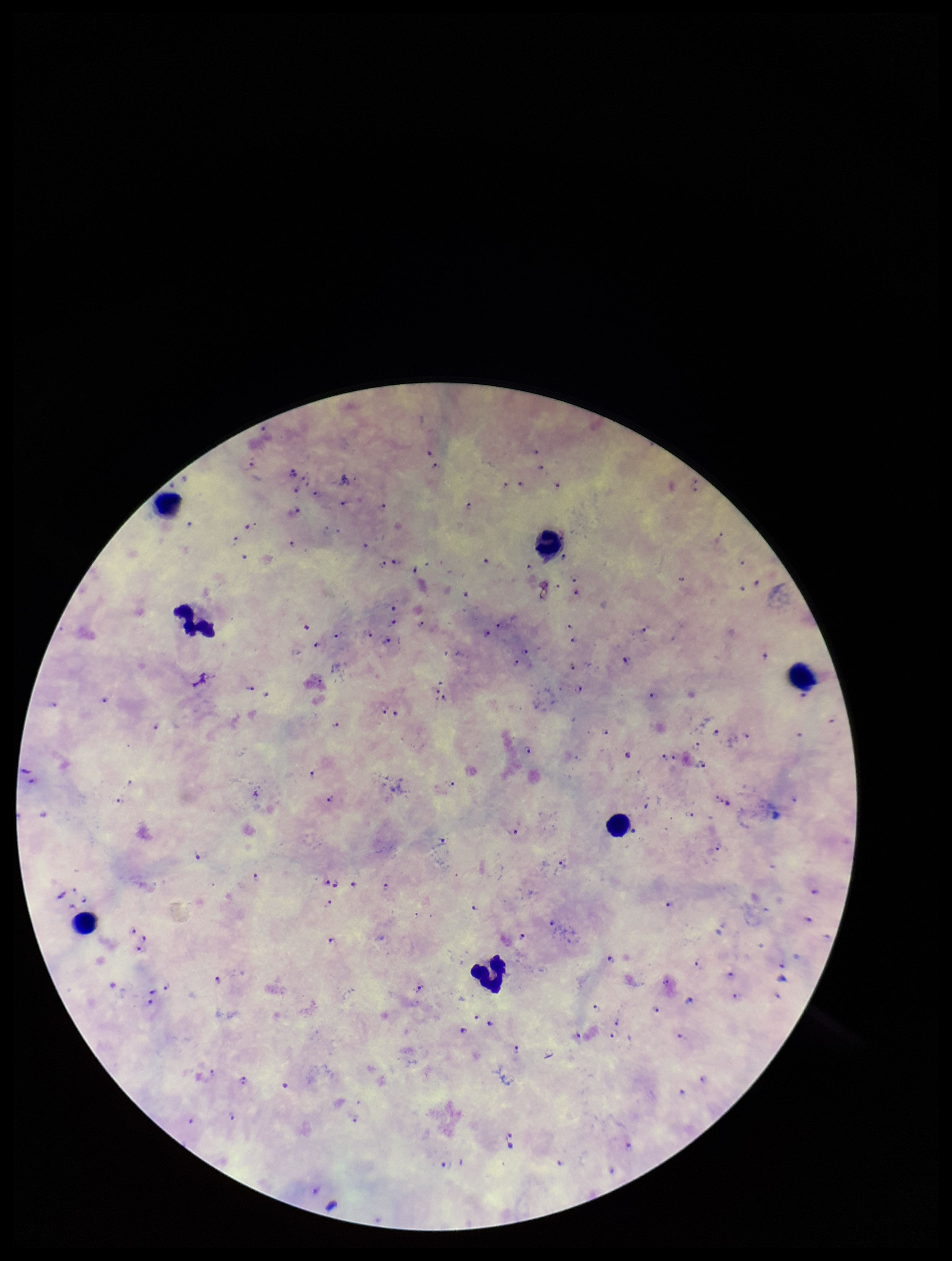
Summary:
  - Patient malaria status: infected
  - Plasmodium parasites: identified
  - Preparation: thick blood smear
  - Field of view: single
  - Parasite count: 120
  - Stain: Giemsa
  - Leukocyte count: 7
  - Image size: 952×1261 pixels
  - Capture: smartphone photograph through the microscope eyepiece
  - Species reported for this patient: Plasmodium falciparum